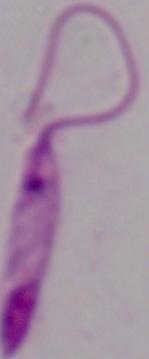

magnification: 1000x
identification: Leishmania
modality: micrograph